Comment on the morphology of the erythrocytes.
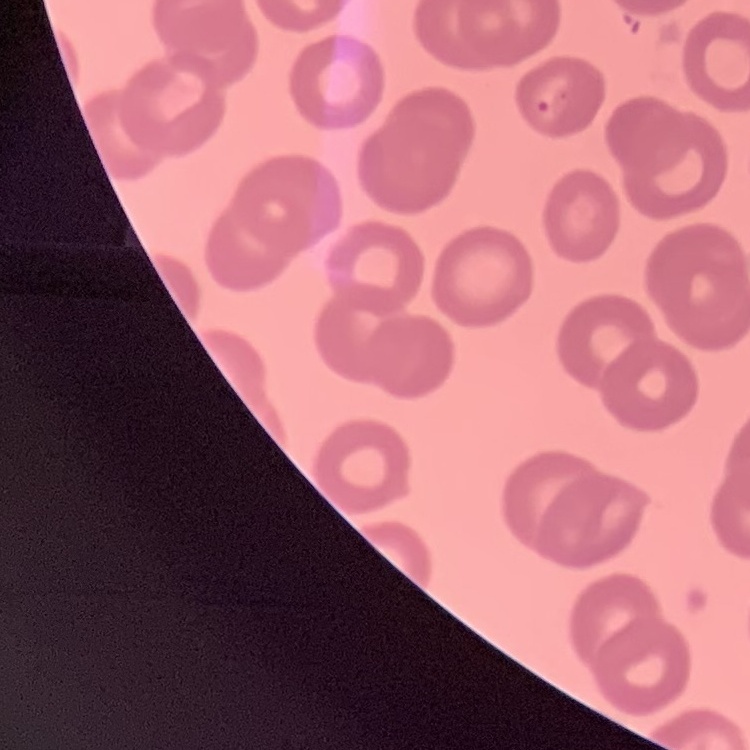
They show no rouleaux formation.

Square crop of a larger photomicrograph. Thin blood smear. Stained with either Field's or Giemsa.